Name the parasite shown.
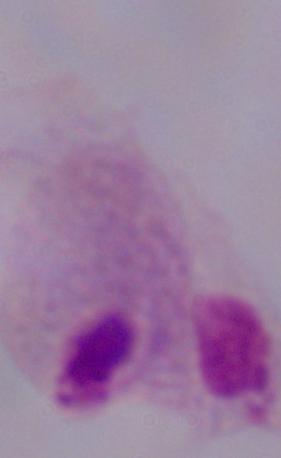
A trichomonad.

Photomicrograph. Captured at 1000x magnification.